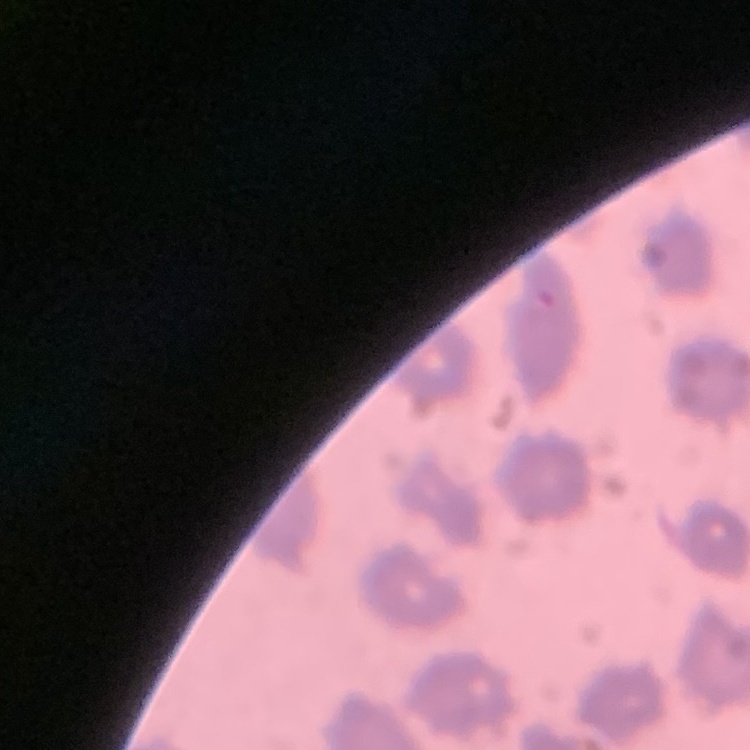
red blood cell morphology = no rouleaux formation
stain = Field's or Giemsa
preparation = thin blood film
image type = one tile cut from a larger photomicrograph